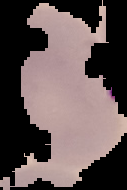
Result: malaria parasites detected. Segmented cell region on a black background. From a thin blood smear. Image is 127×190 pixels.